Outline each blood parasite and name the species.
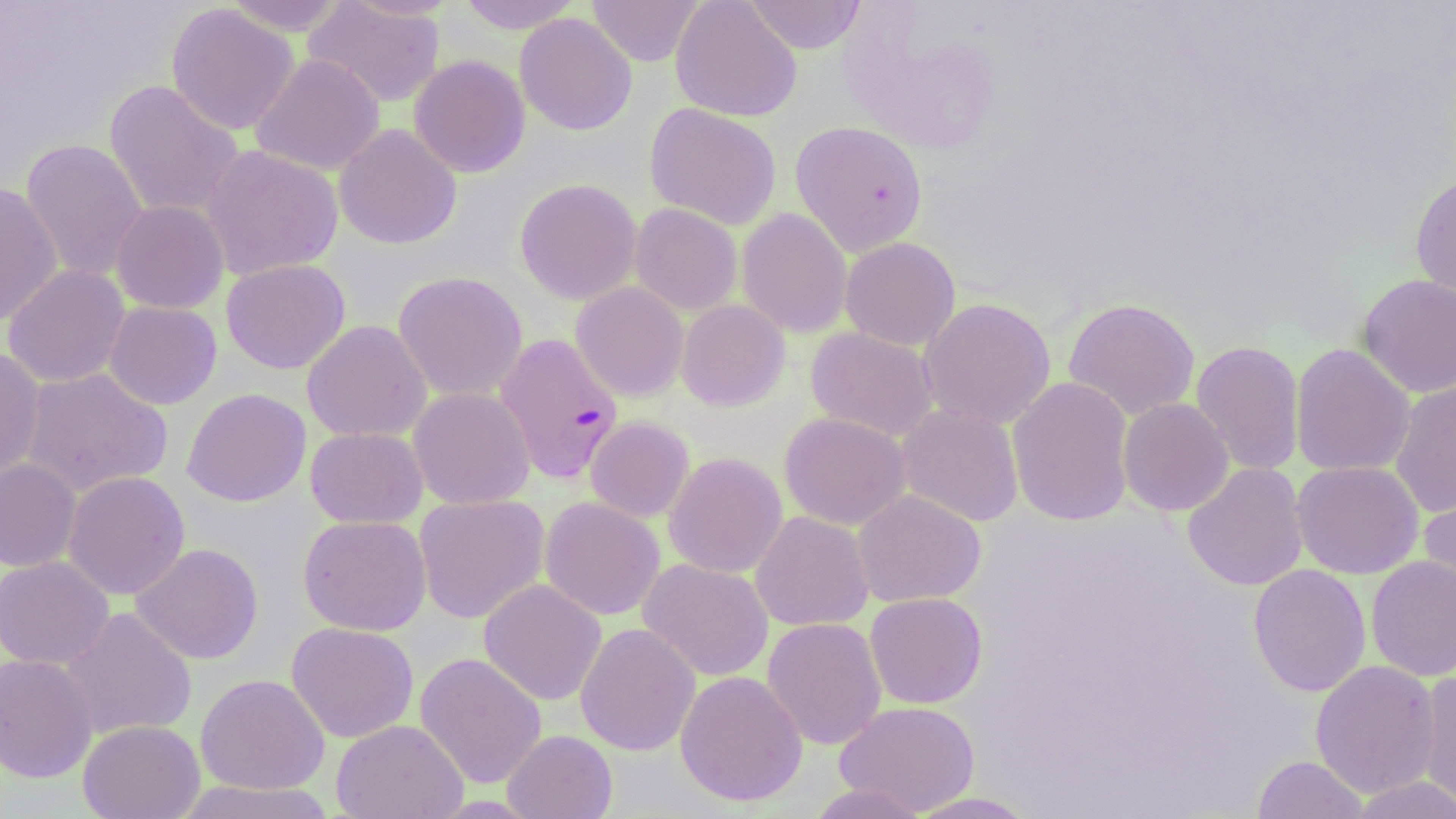
Approximate bounding boxes as [x1, y1, x2, y2] in pixels.
Plasmodium falciparum-infected red blood cells: [494, 332, 623, 484].
No Plasmodium ovale, Plasmodium malariae, Plasmodium vivax, Babesia divergens, or Trypanosoma brucei observed.

Uninfected red blood cell locations: [219, 0, 352, 35], [303, 0, 446, 107], [456, 0, 583, 34], [587, 0, 705, 66], [670, 0, 802, 122], [745, 0, 866, 54], [165, 4, 300, 135], [838, 6, 1004, 156], [515, 13, 636, 136], [250, 53, 384, 175], [409, 55, 531, 178], [104, 80, 244, 220], [644, 103, 782, 230], [790, 120, 929, 256], [334, 124, 461, 249], [20, 138, 148, 283], [201, 144, 343, 281], [1409, 173, 1456, 310], [515, 178, 641, 304], [0, 182, 63, 326], [111, 200, 229, 313], [630, 203, 742, 315], [736, 208, 852, 338], [840, 237, 960, 351], [221, 259, 351, 374], [3, 264, 130, 387], [393, 271, 528, 402], [1356, 273, 1456, 397], [571, 282, 689, 401], [918, 297, 1056, 429], [1063, 298, 1200, 419], [676, 299, 790, 411], [104, 301, 222, 409], [301, 320, 431, 442], [805, 327, 939, 441], [1190, 339, 1305, 477], [1290, 343, 1416, 477], [0, 347, 46, 483], [19, 366, 173, 498], [1007, 376, 1135, 527], [1389, 379, 1456, 518], [408, 387, 535, 509], [182, 388, 311, 507], [1117, 397, 1234, 516], [897, 404, 1024, 527], [779, 411, 910, 530], [585, 416, 694, 523], [305, 426, 428, 529], [664, 452, 787, 578], [0, 459, 81, 572], [1291, 460, 1424, 579], [1182, 462, 1308, 591], [62, 471, 190, 600], [1419, 482, 1456, 607], [853, 489, 985, 607], [414, 494, 550, 624], [540, 497, 665, 620], [750, 511, 874, 631], [297, 514, 432, 635], [130, 543, 264, 664], [0, 555, 114, 670], [1366, 556, 1456, 680], [637, 558, 775, 682], [1249, 564, 1371, 697], [478, 579, 607, 706], [865, 592, 987, 708], [58, 608, 197, 741], [762, 617, 887, 750], [286, 622, 419, 743], [575, 622, 701, 755], [415, 652, 547, 789], [0, 653, 99, 783], [1310, 660, 1441, 798], [675, 670, 807, 806], [1415, 671, 1456, 813], [195, 673, 329, 795], [834, 700, 980, 816], [78, 719, 204, 819], [331, 719, 468, 819], [502, 730, 617, 819], [1252, 755, 1370, 818], [1350, 776, 1456, 818], [174, 779, 336, 818], [807, 782, 930, 819], [903, 791, 1040, 818]. Slide-level diagnosis: Plasmodium falciparum. One field of a larger specimen. Thin blood smear. May-Grünwald-Giemsa stain. Light microscopy. 1000x magnification. Image is 1456×819 pixels.